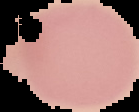
image size = 139×112 pixels
preparation = thin blood film
image type = cell region segmented out of the field of view; surrounding area masked to black
result = no Plasmodium parasites seen